Give the extent of all Plasmodium ovale-infected red blood cells.
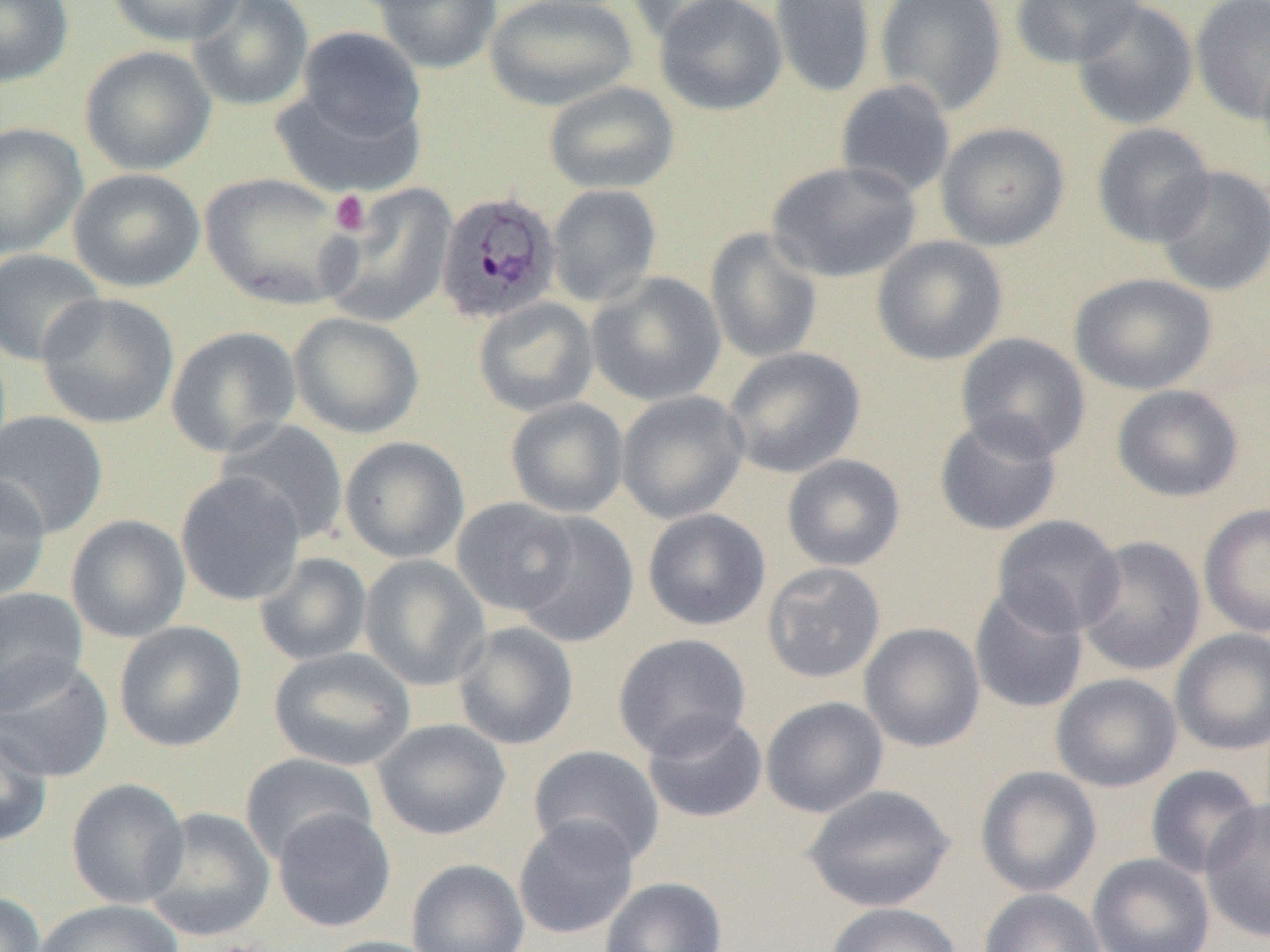

Approximate bounding boxes as (x1,y1)-(x2,y2) corner pairs in pixels.
Plasmodium ovale-infected red blood cells: (435,190)-(560,324).

slide-level diagnosis = Plasmodium ovale
uninfected red blood cell locations = approximate bounding boxes as (x1,y1)-(x2,y2) corner pairs in pixels: (0,0)-(74,87), (106,0)-(247,46), (187,0)-(314,112), (371,0)-(502,74), (484,0)-(638,111), (623,0)-(749,44), (654,0)-(788,116), (770,0)-(876,99), (875,0)-(1007,116), (1010,0)-(1146,68), (1190,0)-(1270,123), (1071,1)-(1199,130), (296,26)-(425,142), (79,44)-(217,175), (1256,50)-(1270,171), (834,79)-(956,201), (543,81)-(680,195), (271,87)-(424,199), (0,122)-(88,259), (935,122)-(1070,250), (1091,123)-(1216,249), (766,159)-(922,283), (1154,166)-(1270,297), (68,167)-(206,292), (200,172)-(356,310), (546,183)-(662,307), (320,184)-(459,329), (705,227)-(823,364), (871,235)-(1008,365), (0,248)-(105,366), (586,271)-(726,406), (1069,272)-(1217,395), (36,292)-(180,429), (473,297)-(599,417), (288,312)-(424,440), (166,325)-(302,458), (955,333)-(1091,462), (723,346)-(866,478), (1111,384)-(1244,502), (616,390)-(750,524), (505,397)-(629,518), (0,410)-(109,539), (933,414)-(1063,536), (217,420)-(350,546), (339,436)-(470,564), (782,454)-(906,571), (175,472)-(307,607), (0,473)-(51,605), (451,497)-(580,617), (1199,503)-(1270,637), (643,508)-(771,631), (513,512)-(639,647), (66,514)-(191,643), (991,514)-(1125,638), (1076,536)-(1205,676), (254,552)-(373,666), (359,555)-(491,692), (762,562)-(886,684), (968,585)-(1089,713), (0,587)-(89,713), (113,620)-(247,752), (453,621)-(579,750), (859,622)-(986,752), (1170,628)-(1270,756), (613,633)-(751,759), (268,646)-(416,771), (0,655)-(114,783), (1051,673)-(1182,792), (760,696)-(889,818), (642,710)-(768,823), (372,719)-(512,840), (0,724)-(53,848), (528,744)-(665,867), (240,753)-(379,865), (1145,765)-(1263,879), (975,766)-(1102,897), (66,778)-(191,909), (801,784)-(956,912), (1200,797)-(1270,943), (143,807)-(276,942), (272,808)-(396,932), (513,815)-(640,939), (1088,853)-(1215,952), (407,859)-(530,952), (599,876)-(727,952), (979,889)-(1106,952), (0,892)-(45,952), (33,899)-(185,952), (825,902)-(963,952), (314,935)-(449,952)
image size = 1270×952 pixels
magnification = 1000x
platelet locations = approximate bounding boxes as (x1,y1)-(x2,y2) corner pairs in pixels: (329,190)-(372,236)
field of view = one of a larger specimen
modality = optical microscopy
preparation = thin blood smear